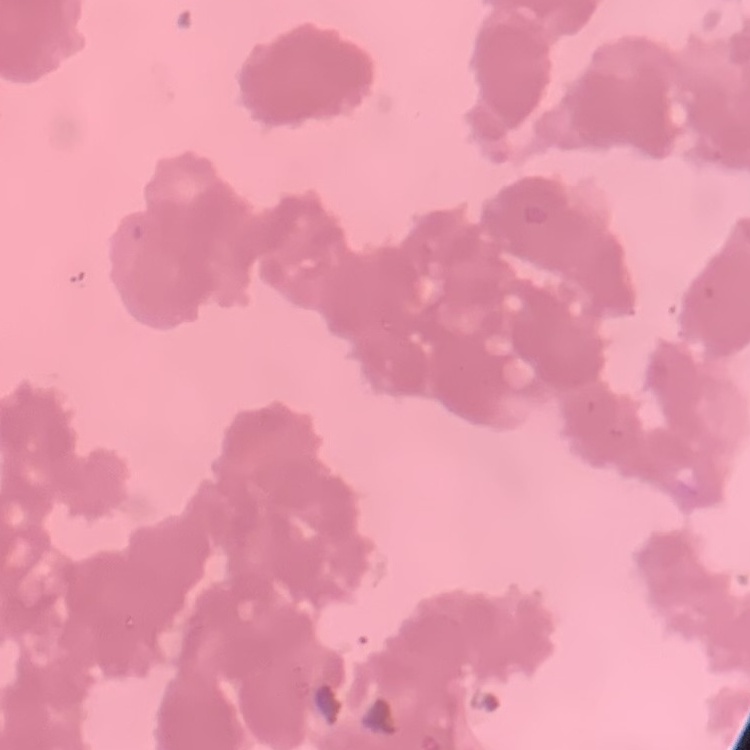

erythrocyte_morphology: rouleaux formation
image_type: one tile cut from a larger photomicrograph
stain: Field's or Giemsa
preparation: thin blood smear